Locate every white blood cell.
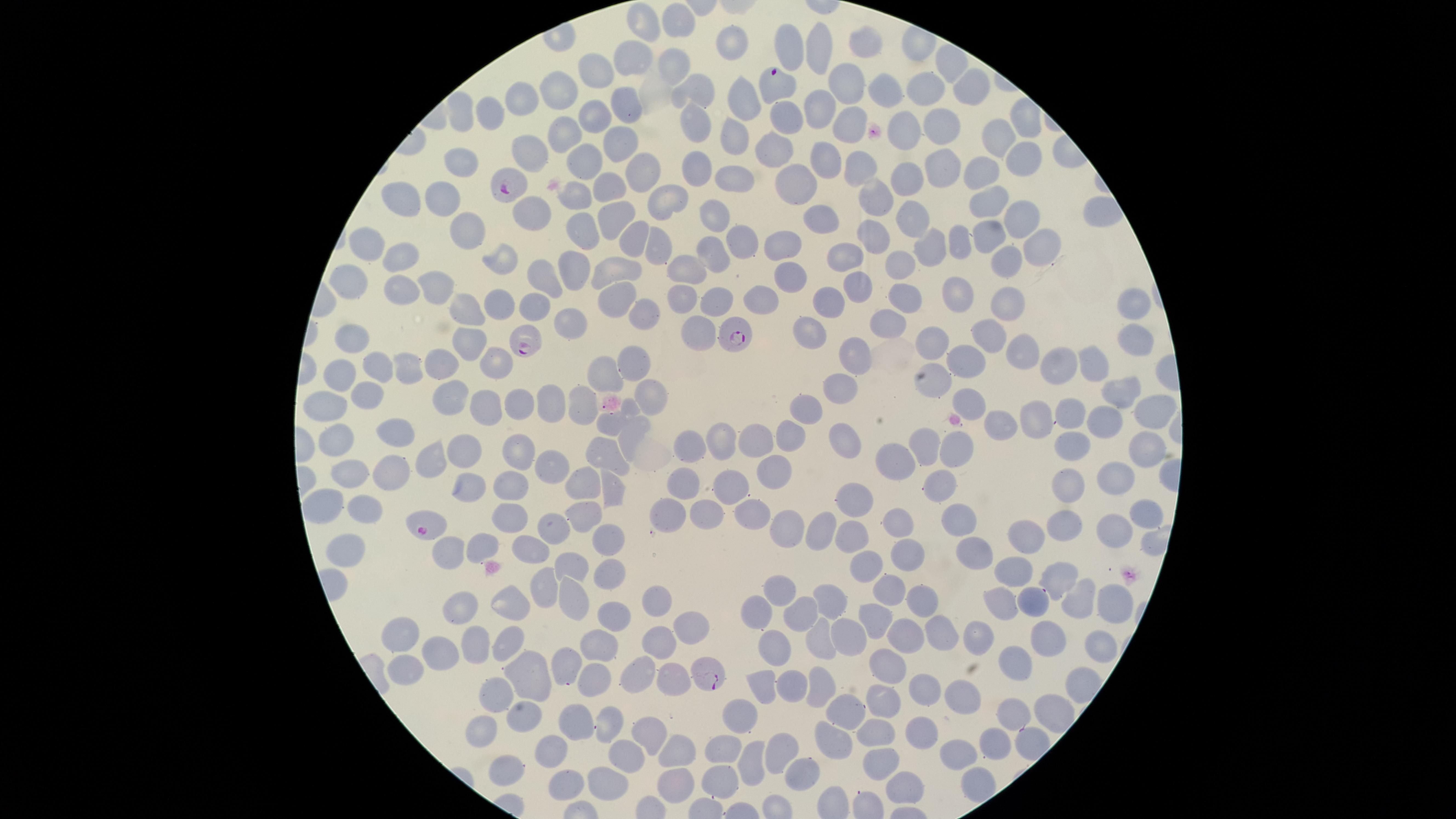
No white blood cells identified.

Approximate marker points as (x, y) in pixels.
Summary:
  - Parasitized red blood cells: (781, 84), (512, 191), (733, 339), (523, 342), (428, 529), (712, 678)
  - Uninfected red blood cells: (649, 22), (678, 23), (732, 44), (866, 49), (821, 53), (636, 58), (946, 65), (669, 66), (591, 73), (843, 82), (565, 84), (919, 87), (970, 90), (691, 92), (887, 93), (734, 96), (521, 97), (620, 101), (821, 104), (464, 113), (490, 114), (598, 115), (694, 118), (784, 118), (851, 119), (936, 126), (736, 129), (569, 131), (999, 131), (902, 132), (619, 141), (529, 146), (1016, 154), (771, 157), (830, 158), (465, 161), (589, 162), (860, 166), (638, 169), (938, 170), (696, 171), (979, 172), (736, 176), (796, 180), (912, 181), (613, 187), (877, 194), (447, 195), (404, 199), (574, 202), (989, 202), (658, 204), (712, 211), (616, 212), (531, 213), (913, 215), (819, 220), (1014, 222), (467, 233), (872, 233), (581, 235), (740, 238), (626, 239), (987, 240), (654, 241), (959, 241), (783, 242), (370, 244), (931, 246), (1043, 246), (846, 252), (718, 254), (407, 255), (905, 260), (497, 262), (1009, 262), (575, 267), (624, 267), (693, 267), (788, 279), (548, 280), (349, 284), (433, 285), (858, 285), (401, 290), (957, 293), (904, 296), (680, 297), (762, 298), (828, 298), (614, 300), (714, 301), (1008, 301), (500, 302), (534, 302), (1128, 303), (640, 309), (467, 313), (882, 319), (567, 325), (695, 329), (808, 331), (355, 335), (989, 340), (1132, 340), (930, 344), (470, 347), (857, 350), (1021, 351), (436, 356), (965, 358), (491, 362), (1089, 362), (633, 363), (1049, 363), (371, 366), (399, 368), (342, 371), (600, 375), (928, 378), (838, 385), (1119, 392), (362, 394), (450, 395), (650, 398), (971, 401), (547, 403), (316, 404), (577, 405), (514, 406), (811, 406), (1150, 409), (1073, 411), (482, 412), (1040, 416), (1005, 419), (607, 423), (1104, 424), (386, 429), (628, 437), (787, 437), (754, 439), (335, 442), (848, 442), (1069, 442), (928, 444), (721, 445), (513, 448), (690, 448), (1142, 448), (458, 450), (605, 450), (949, 450), (431, 458), (899, 458), (543, 461), (773, 466), (345, 467), (381, 474), (1111, 478), (579, 481), (616, 482), (933, 484), (1064, 484), (680, 485), (509, 487), (462, 489), (722, 491), (852, 499), (323, 507), (753, 508), (357, 509), (703, 509), (665, 511), (1138, 513), (580, 516), (951, 516), (890, 519), (507, 520), (1059, 521), (824, 523), (787, 524), (1104, 525), (552, 532), (1027, 532), (607, 535), (850, 536), (479, 544), (350, 547), (527, 550), (967, 554), (907, 558), (437, 559), (573, 561), (870, 569), (1012, 569), (604, 570), (1050, 578), (540, 586), (889, 587), (778, 589), (569, 593), (655, 597), (919, 598), (1077, 598), (996, 599), (1034, 599), (827, 602), (1107, 602), (505, 603), (756, 611), (461, 612), (614, 612), (798, 613), (874, 619), (698, 623), (936, 630), (849, 633), (400, 635), (905, 636), (816, 637), (975, 638), (511, 642), (602, 642), (656, 643), (772, 643), (1047, 643), (474, 644), (1099, 648), (438, 653), (570, 661), (1012, 661), (884, 662), (408, 671), (526, 674), (637, 675), (591, 679), (672, 679), (763, 681), (791, 682), (821, 685), (923, 688), (497, 695), (956, 699), (884, 702), (1041, 708), (839, 712), (740, 714), (521, 717), (605, 717), (1014, 718), (570, 724), (876, 725), (483, 728), (923, 733), (644, 736), (828, 737), (991, 742), (724, 743), (679, 747), (776, 748), (963, 755), (883, 757), (551, 758), (621, 759), (745, 760), (722, 771), (501, 773), (800, 774), (974, 777), (673, 782), (902, 782), (607, 784), (565, 789)
  - Preparation: thin smear of blood
  - Capture: smartphone photograph through the microscope eyepiece
  - Field of view: single
  - Image size: 1456×819 pixels
  - Stain: Giemsa
  - Visible region: circular
  - Presence: malaria parasites detected
  - Species: Plasmodium falciparum